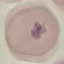
Malaria status: parasitized. Photographed with a smartphone camera at the microscope eyepiece. Giemsa-stained preparation. Thin blood smear. Automatically extracted cell patch, resized to 64 × 64 pixels.